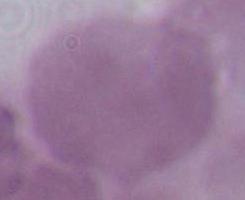

Captured at 1000x magnification. Photomicrograph. A red blood cell is seen.